Report the malaria status of this cell.
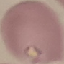
It is uninfected.

{
  "image_type": "cell patch, automatically extracted from a larger field of view and resized to 64 × 64 pixels",
  "capture": "smartphone through the microscope eyepiece",
  "stain": "Giemsa",
  "preparation": "thin smear"
}